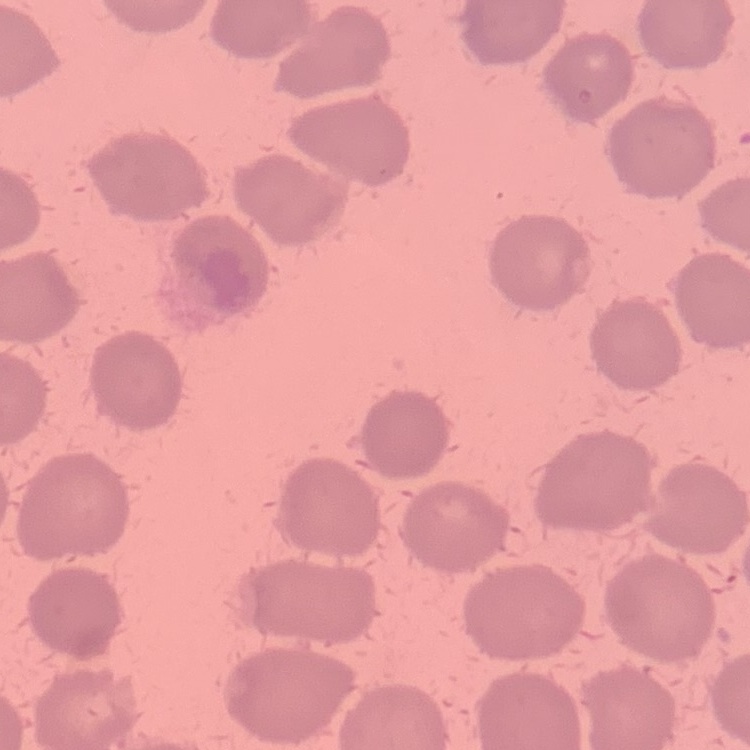

red blood cell morphology = no rouleaux formation
image type = one tile cut from a larger photomicrograph
preparation = thin peripheral smear
stain = Field's or Giemsa